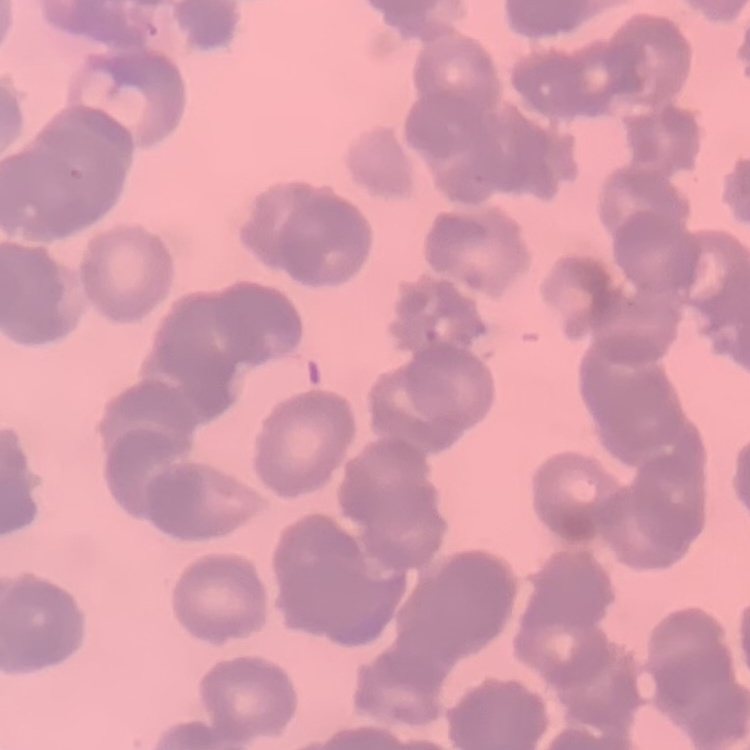
The red blood cells exhibit rouleaux formation. One tile cut from a larger photomicrograph. Thin blood smear. Stained with either Field's or Giemsa.